Report the malaria status of this cell.
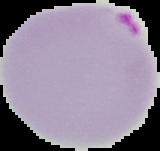
Parasitized.

From a thin blood film. Image is 160×151 pixels. Segmented cell region on a black background.